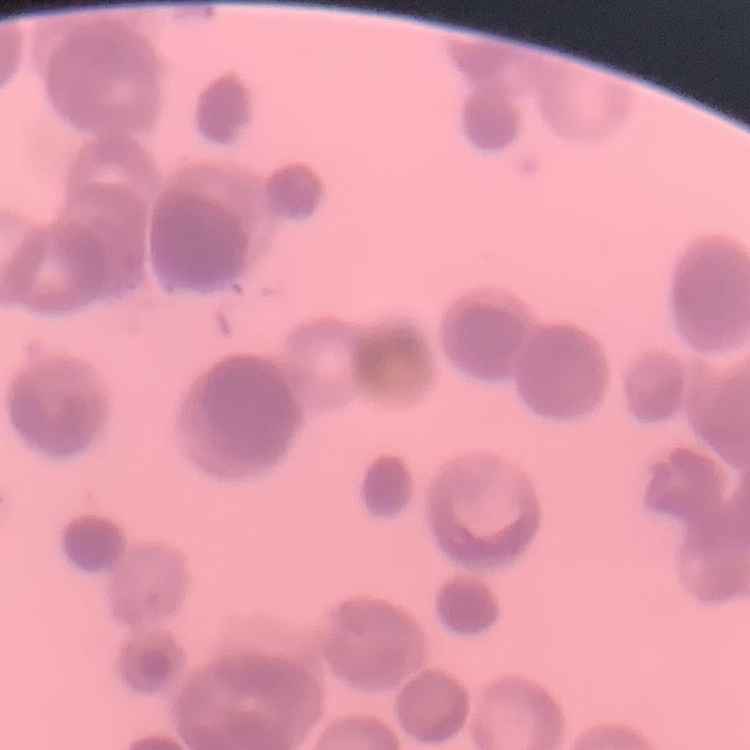

The erythrocytes exhibit rouleaux formation. Stained with either Field's or Giemsa. Thin blood film. One tile cut from a larger photomicrograph.